Classify this cell by malaria status.
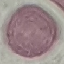
Uninfected.

stain = Giemsa
image type = automatically extracted cell patch, resized to 64 × 64 pixels
preparation = thin blood smear
capture = smartphone through the microscope eyepiece